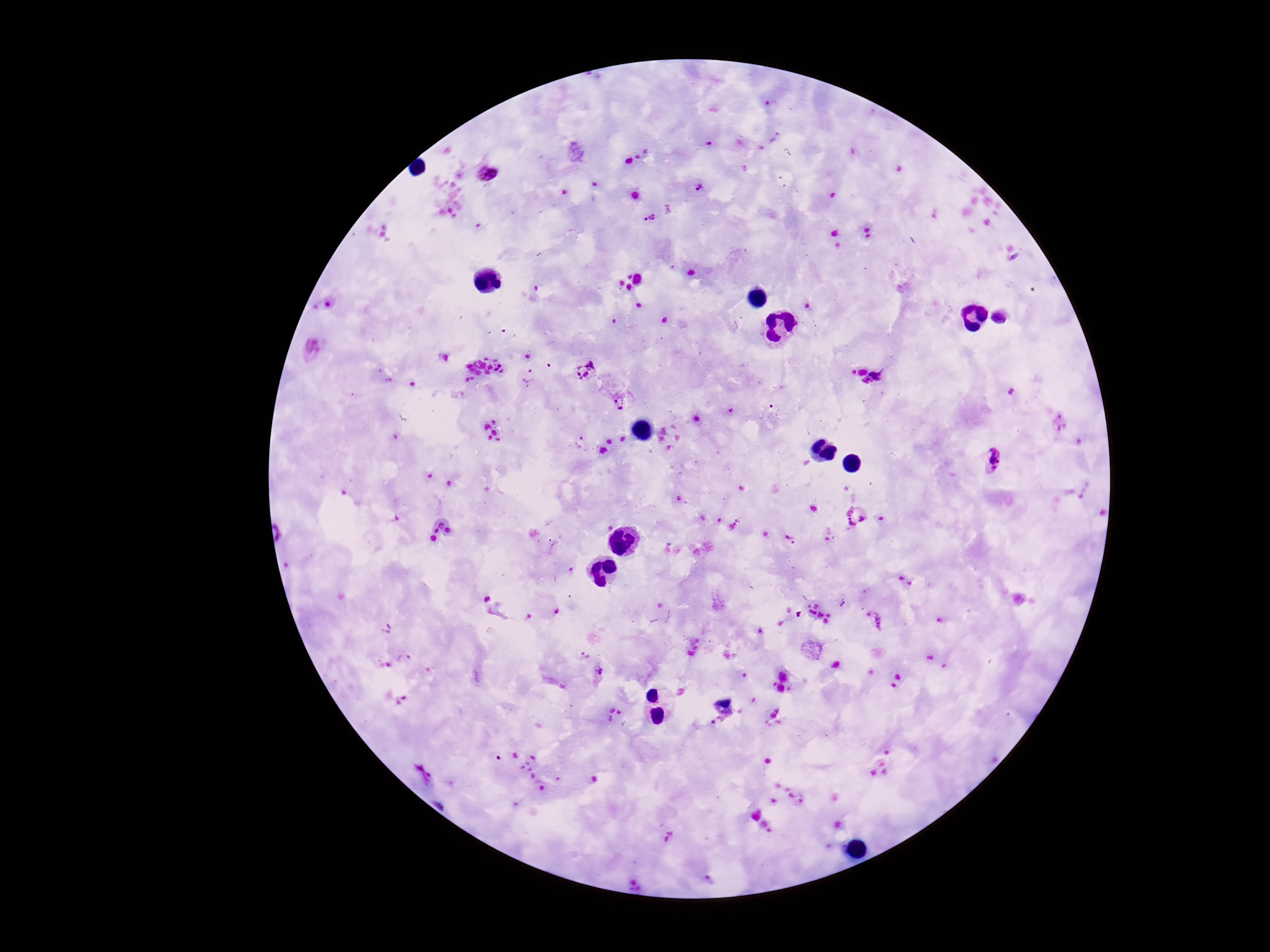
Approximate centers as {x, y} in pixels.
Summary:
  - Plasmodium parasite locations: {485, 173}, {701, 187}, {649, 218}, {585, 370}, {529, 375}, {868, 375}, {1013, 392}, {620, 403}, {991, 462}, {856, 518}, {789, 539}, {842, 603}, {875, 621}, {599, 674}
  - Patient malaria status: infected
  - Capture: smartphone camera through the microscope eyepiece
  - Magnification: 100x
  - Field of view: single
  - Preparation: thick blood smear
  - Image size: 1270×952 pixels
  - Stain: Giemsa